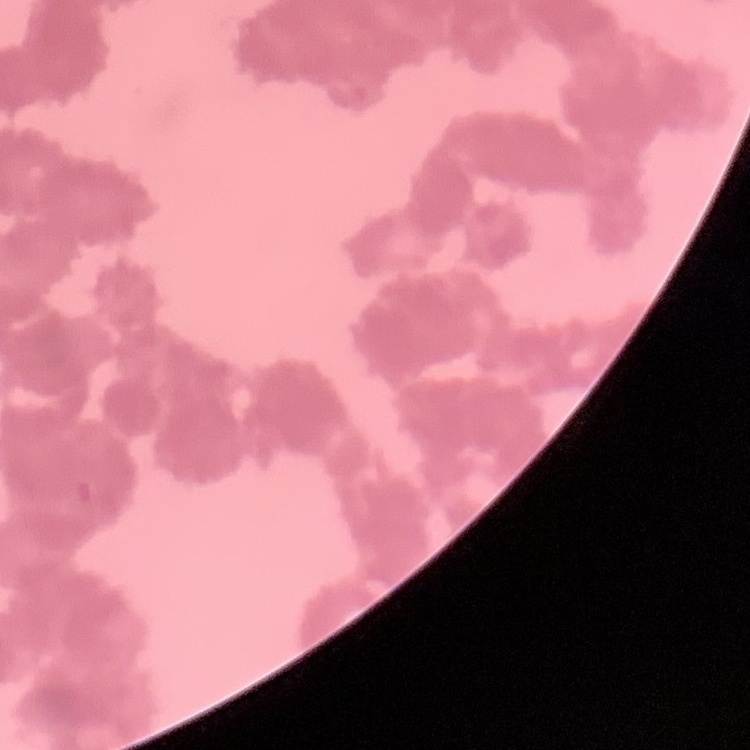
Summary:
  - Red blood cell morphology: rouleaux formation
  - Preparation: thin blood smear
  - Image type: square crop of a larger photomicrograph
  - Stain: Field's or Giemsa